Identify the cell.
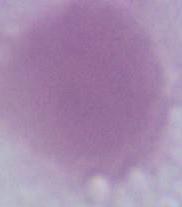
This is an erythrocyte.

Micrograph. Captured at 1000x magnification.